Describe the morphology of the red blood cells.
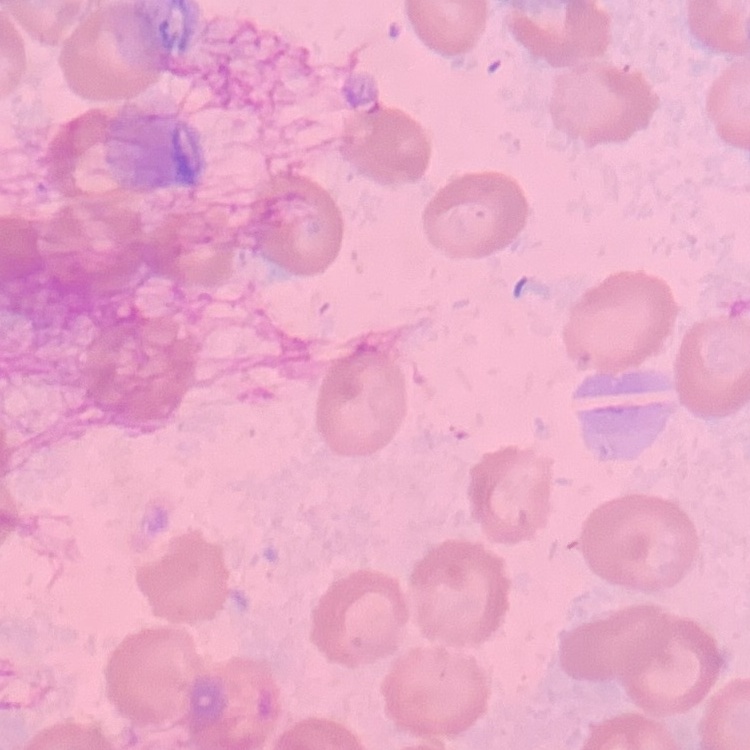

They show no rouleaux formation.

stain = Field's or Giemsa
preparation = thin blood film
image type = one tile cut from a larger photomicrograph